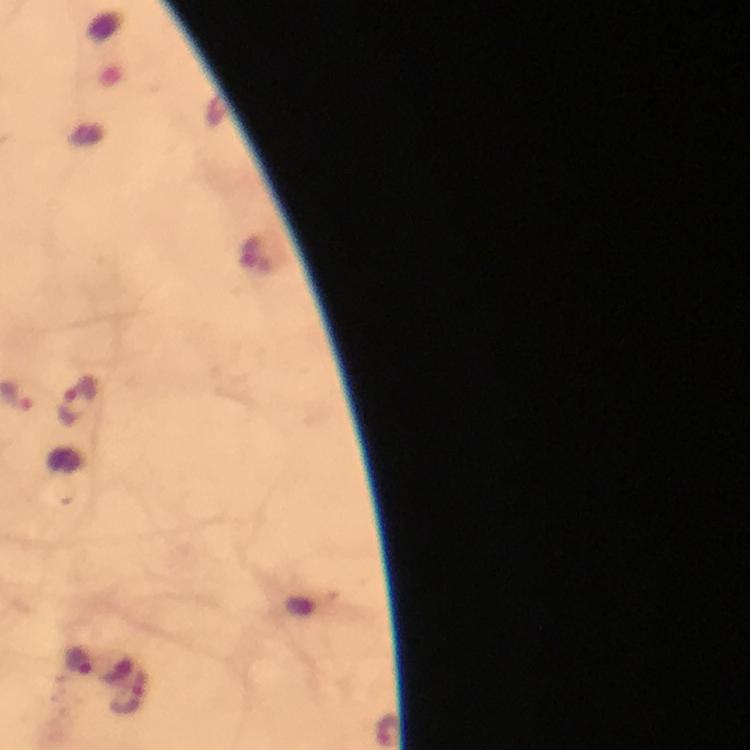
context = from a diagnostic examination for malaria
stain = Giemsa
preparation = thick smear
capture = smartphone photograph through a microscope
immersion oil = applied
magnification = 100x
image size = 750×750 pixels
Plasmodium parasite locations = approximate centers as [x, y] in pixels: [80, 402], [77, 659]
cropped from = a single field of view